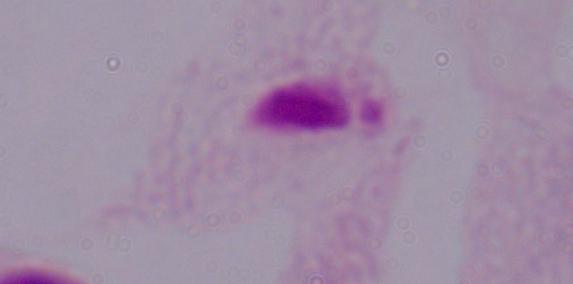 1000x magnification. Micrograph. A trichomonad is seen.